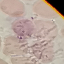

Result: no malaria parasites detected. Giemsa-stained preparation. Acquired by smartphone through the microscope eyepiece. Thin smear of blood. Cell patch, automatically extracted from a larger field of view and resized to 64 × 64 pixels.